Outline each Plasmodium falciparum-infected red blood cell.
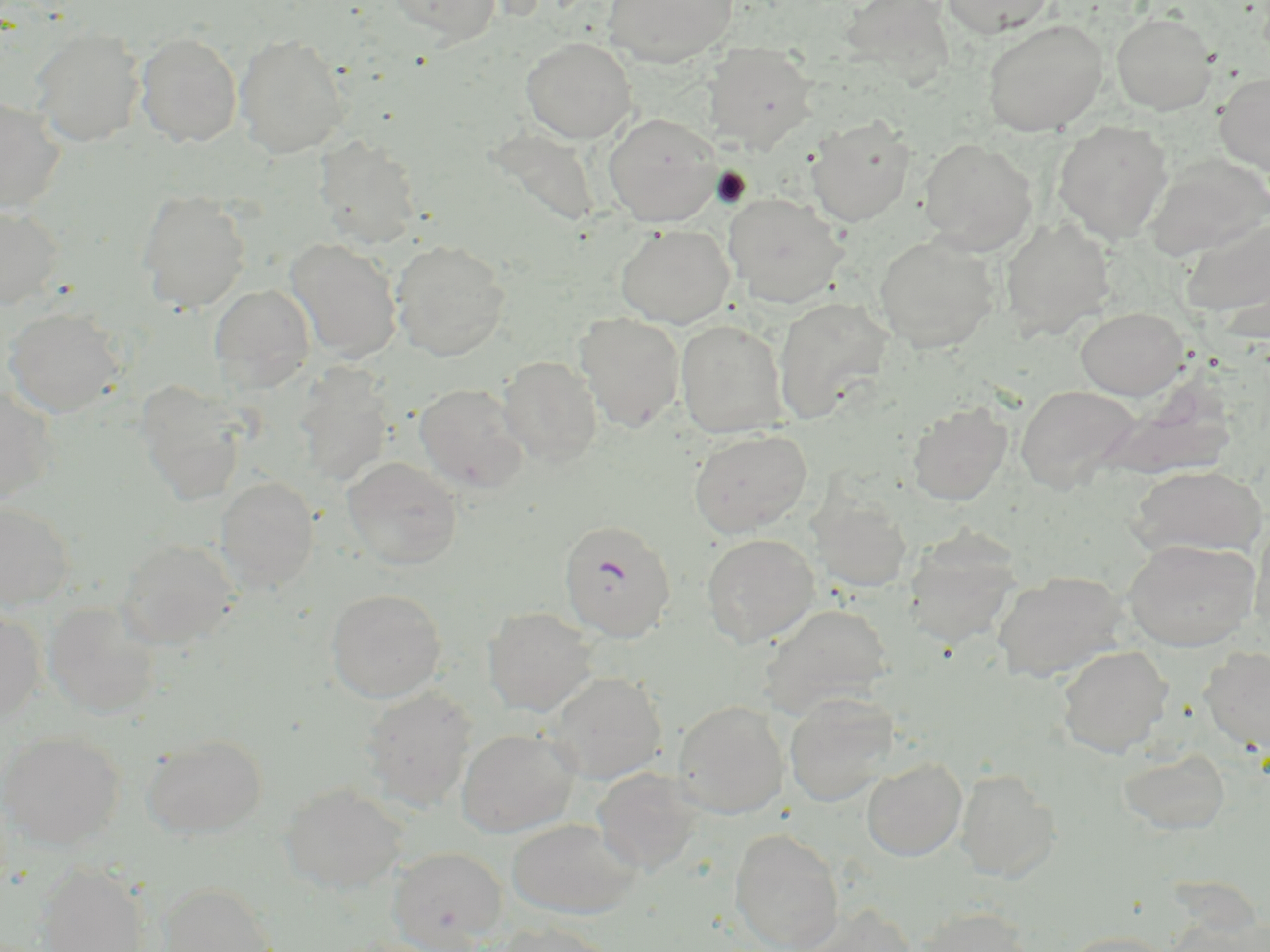

Approximate bounding boxes as named x1/y1/x2/y2 corners in pixels.
Plasmodium falciparum-infected red blood cells: (x1=558, y1=519, x2=677, y2=643).

Summary:
  - Uninfected red blood cell locations: (x1=388, y1=0, x2=501, y2=44), (x1=603, y1=0, x2=739, y2=67), (x1=844, y1=0, x2=954, y2=92), (x1=941, y1=0, x2=1056, y2=38), (x1=1111, y1=12, x2=1218, y2=115), (x1=982, y1=19, x2=1108, y2=137), (x1=29, y1=27, x2=145, y2=146), (x1=135, y1=31, x2=243, y2=147), (x1=235, y1=32, x2=350, y2=159), (x1=521, y1=36, x2=636, y2=143), (x1=704, y1=42, x2=818, y2=151), (x1=1215, y1=71, x2=1270, y2=176), (x1=0, y1=97, x2=66, y2=214), (x1=603, y1=113, x2=722, y2=226), (x1=806, y1=118, x2=915, y2=227), (x1=494, y1=121, x2=603, y2=233), (x1=1052, y1=121, x2=1173, y2=243), (x1=316, y1=137, x2=422, y2=249), (x1=919, y1=138, x2=1037, y2=253), (x1=1144, y1=153, x2=1270, y2=261), (x1=137, y1=190, x2=251, y2=313), (x1=723, y1=193, x2=847, y2=307), (x1=0, y1=205, x2=63, y2=310), (x1=999, y1=217, x2=1116, y2=340), (x1=1183, y1=218, x2=1269, y2=322), (x1=616, y1=224, x2=734, y2=328), (x1=874, y1=234, x2=1000, y2=353), (x1=286, y1=239, x2=403, y2=363), (x1=390, y1=240, x2=510, y2=362), (x1=210, y1=284, x2=316, y2=392), (x1=773, y1=297, x2=893, y2=422), (x1=3, y1=307, x2=126, y2=418), (x1=1074, y1=307, x2=1189, y2=400), (x1=575, y1=312, x2=685, y2=432), (x1=675, y1=319, x2=790, y2=438), (x1=498, y1=356, x2=602, y2=466), (x1=1094, y1=361, x2=1236, y2=484), (x1=293, y1=364, x2=395, y2=487), (x1=136, y1=383, x2=246, y2=504), (x1=414, y1=383, x2=528, y2=494), (x1=1015, y1=384, x2=1140, y2=493), (x1=0, y1=385, x2=57, y2=508), (x1=907, y1=401, x2=1013, y2=506), (x1=688, y1=428, x2=813, y2=538), (x1=342, y1=457, x2=463, y2=571), (x1=1128, y1=465, x2=1267, y2=559), (x1=215, y1=476, x2=319, y2=591), (x1=810, y1=495, x2=913, y2=593), (x1=0, y1=501, x2=75, y2=609), (x1=1250, y1=518, x2=1270, y2=635), (x1=903, y1=528, x2=1021, y2=650), (x1=701, y1=532, x2=820, y2=649), (x1=115, y1=538, x2=238, y2=650), (x1=1123, y1=538, x2=1260, y2=651), (x1=993, y1=570, x2=1128, y2=683), (x1=326, y1=588, x2=446, y2=703), (x1=43, y1=602, x2=161, y2=719), (x1=760, y1=603, x2=895, y2=717), (x1=483, y1=607, x2=598, y2=716), (x1=0, y1=608, x2=45, y2=723), (x1=1056, y1=645, x2=1173, y2=758), (x1=1200, y1=646, x2=1269, y2=755), (x1=545, y1=673, x2=668, y2=784), (x1=359, y1=686, x2=477, y2=812), (x1=784, y1=693, x2=898, y2=807), (x1=672, y1=699, x2=790, y2=819), (x1=457, y1=728, x2=579, y2=837), (x1=0, y1=730, x2=125, y2=849), (x1=143, y1=734, x2=266, y2=839), (x1=1118, y1=748, x2=1231, y2=835), (x1=862, y1=757, x2=967, y2=861), (x1=591, y1=767, x2=703, y2=875), (x1=955, y1=768, x2=1061, y2=881), (x1=280, y1=783, x2=408, y2=895), (x1=507, y1=818, x2=641, y2=920), (x1=730, y1=829, x2=844, y2=952), (x1=388, y1=846, x2=508, y2=951), (x1=37, y1=862, x2=151, y2=952), (x1=157, y1=882, x2=275, y2=952), (x1=793, y1=904, x2=919, y2=952), (x1=915, y1=904, x2=1033, y2=952), (x1=490, y1=921, x2=614, y2=952), (x1=1058, y1=930, x2=1176, y2=952)
  - Slide-level diagnosis: Plasmodium falciparum
  - Stain: May-Grünwald-Giemsa
  - Magnification: 1000x
  - Field of view: single
  - Modality: light microscopy
  - Preparation: thin blood smear
  - Image size: 1270×952 pixels